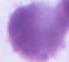
Summary:
  - Identification: erythrocyte
  - Modality: photomicrograph
  - Magnification: 1000x